Identify the cell.
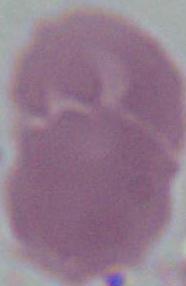

An erythrocyte.

Summary:
  - Magnification: 1000x
  - Modality: photomicrograph